Locate every blood parasite and identify its species.
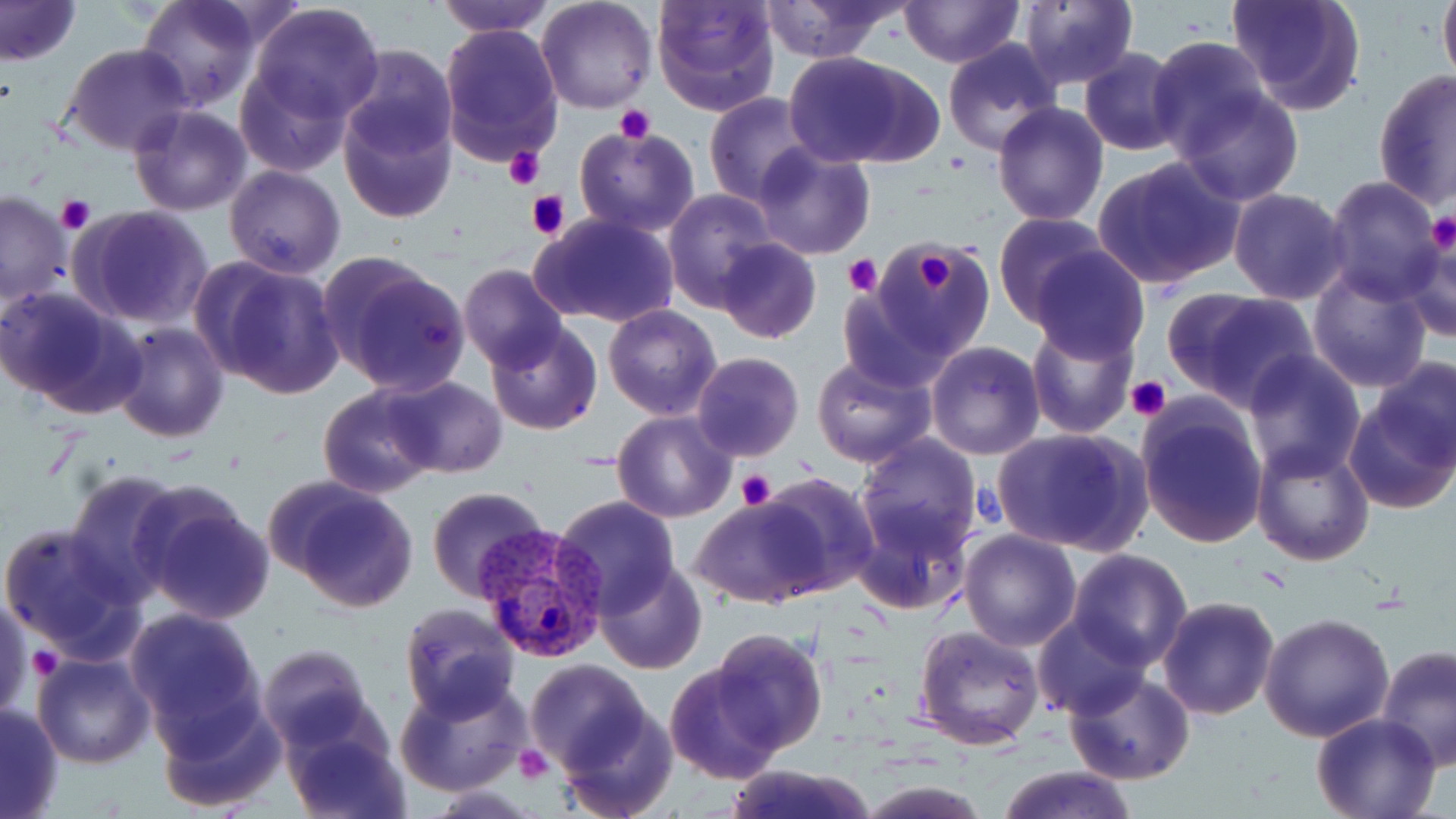

Approximate bounding boxes as (x1, y1, x2, y2) in pixels.
Plasmodium vivax-infected red blood cells: (476, 523, 607, 664).
No Plasmodium falciparum, Plasmodium ovale, Plasmodium malariae, Babesia divergens, or Trypanosoma brucei observed.

{
  "slide_level_diagnosis": "Plasmodium vivax",
  "platelet_locations": "approximate bounding boxes as (x1, y1, x2, y2) in pixels: (615, 104, 654, 143), (503, 146, 544, 190), (527, 189, 571, 239), (56, 195, 95, 235), (1424, 211, 1456, 256), (906, 245, 964, 301), (843, 255, 881, 296), (1126, 376, 1172, 422), (736, 468, 777, 510), (29, 650, 64, 679), (514, 745, 552, 785)",
  "stain": "May-Grünwald-Giemsa",
  "field_of_view": "single",
  "preparation": "thin blood film",
  "magnification": "1000x",
  "uninfected_red_blood_cell_locations": "approximate bounding boxes as (x1, y1, x2, y2) in pixels: (0, 0, 80, 67), (132, 0, 260, 111), (436, 0, 554, 37), (535, 0, 657, 113), (651, 0, 779, 117), (756, 0, 910, 63), (898, 0, 1020, 67), (1227, 0, 1367, 116), (1438, 0, 1456, 90), (1016, 1, 1140, 88), (249, 3, 382, 122), (438, 23, 563, 164), (1147, 36, 1269, 160), (942, 40, 1062, 155), (64, 43, 193, 156), (338, 44, 458, 161), (1077, 48, 1186, 156), (784, 52, 938, 168), (237, 65, 350, 177), (1373, 68, 1455, 210), (1174, 87, 1304, 206), (705, 92, 815, 206), (991, 101, 1109, 226), (128, 105, 252, 217), (337, 106, 456, 225), (574, 124, 699, 239), (751, 144, 876, 259), (1092, 155, 1246, 291), (225, 165, 345, 278), (1322, 175, 1444, 303), (1228, 188, 1352, 306), (0, 191, 72, 305), (662, 191, 775, 310), (70, 206, 214, 330), (531, 213, 679, 329), (994, 213, 1114, 325), (1399, 229, 1456, 341), (716, 238, 820, 344), (874, 242, 995, 358), (1030, 249, 1148, 363), (200, 258, 345, 400), (325, 260, 471, 396), (458, 264, 568, 373), (1308, 265, 1433, 392), (0, 286, 140, 416), (836, 288, 954, 394), (1163, 288, 1319, 411), (603, 304, 721, 419), (485, 320, 603, 436), (1025, 320, 1140, 439), (113, 322, 227, 441), (926, 341, 1045, 460), (1242, 351, 1366, 480), (690, 352, 804, 461), (812, 354, 935, 469), (1366, 355, 1456, 473), (383, 376, 507, 477), (318, 384, 439, 498), (1343, 393, 1456, 516), (1135, 395, 1271, 551), (613, 411, 736, 523), (992, 426, 1151, 557), (854, 436, 982, 557), (1252, 442, 1374, 566), (64, 467, 185, 603), (757, 473, 879, 596), (280, 480, 419, 613), (427, 487, 550, 602), (135, 488, 275, 624), (551, 495, 681, 614), (690, 499, 827, 608), (853, 509, 971, 620), (1, 523, 136, 660), (958, 528, 1082, 652), (1067, 549, 1192, 669), (595, 558, 707, 675), (1072, 567, 1269, 698), (0, 590, 30, 726), (1156, 595, 1280, 719), (398, 602, 520, 720), (124, 607, 266, 744), (1260, 612, 1394, 741), (1035, 614, 1144, 720), (914, 624, 1045, 751), (709, 629, 826, 754), (258, 643, 373, 748), (1375, 645, 1456, 772), (32, 650, 159, 768), (523, 659, 652, 778), (664, 662, 785, 783), (1066, 671, 1195, 787), (395, 677, 530, 798), (155, 695, 286, 813), (1, 702, 64, 819), (555, 704, 678, 819), (1310, 713, 1441, 819), (284, 719, 410, 818), (725, 764, 878, 819), (993, 767, 1136, 819), (856, 779, 991, 819)",
  "image_size": "1456×819 pixels",
  "modality": "optical microscopy"
}